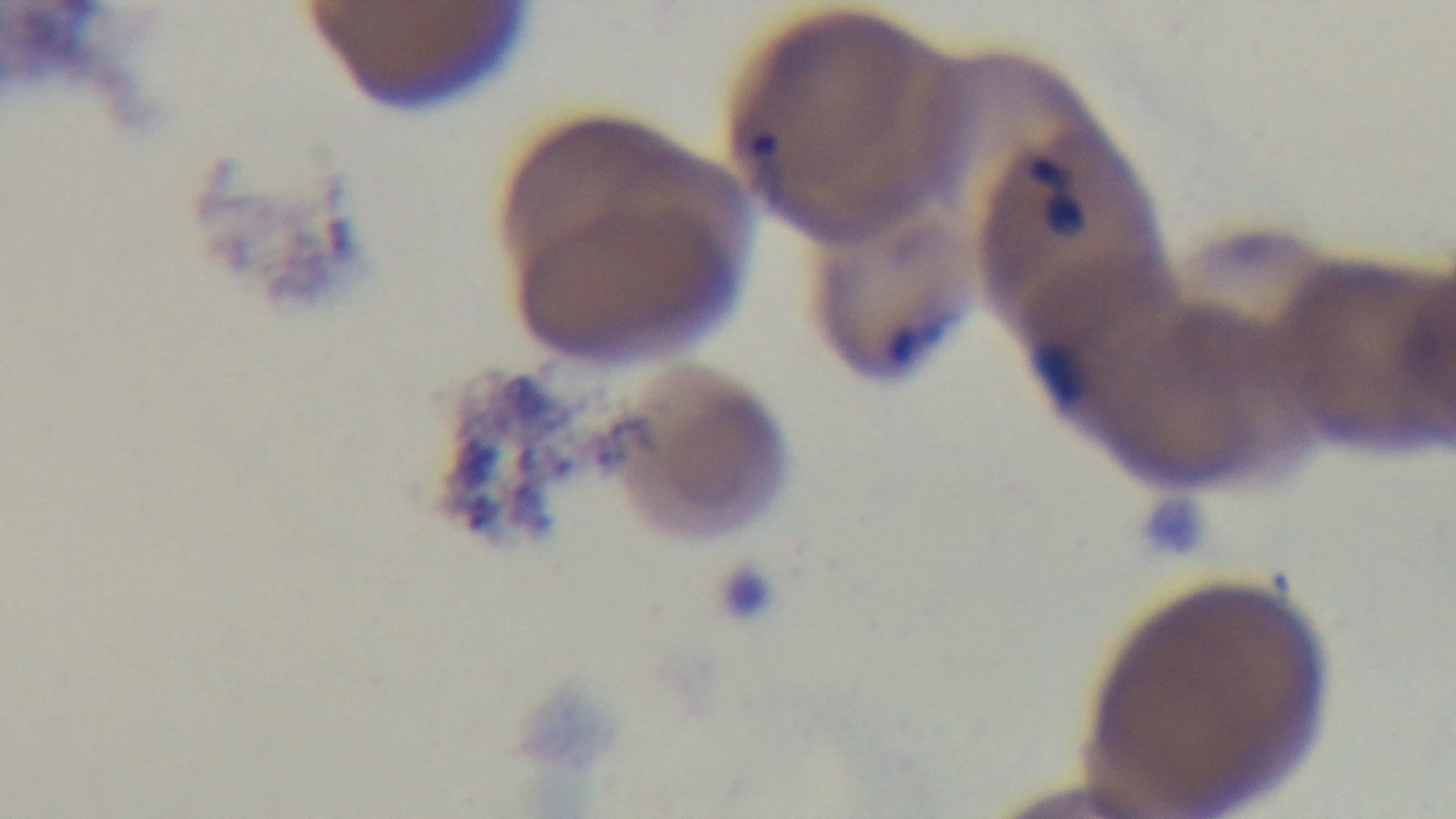
Summary:
  - Stain: Giemsa
  - Preparation: thin blood film
  - Objective: 100x oil immersion
  - Malaria status: positive
  - Modality: light microscopy
  - Capture: mounted 4K digital camera
  - Field of view: one from the slide